Mark where platelets are.
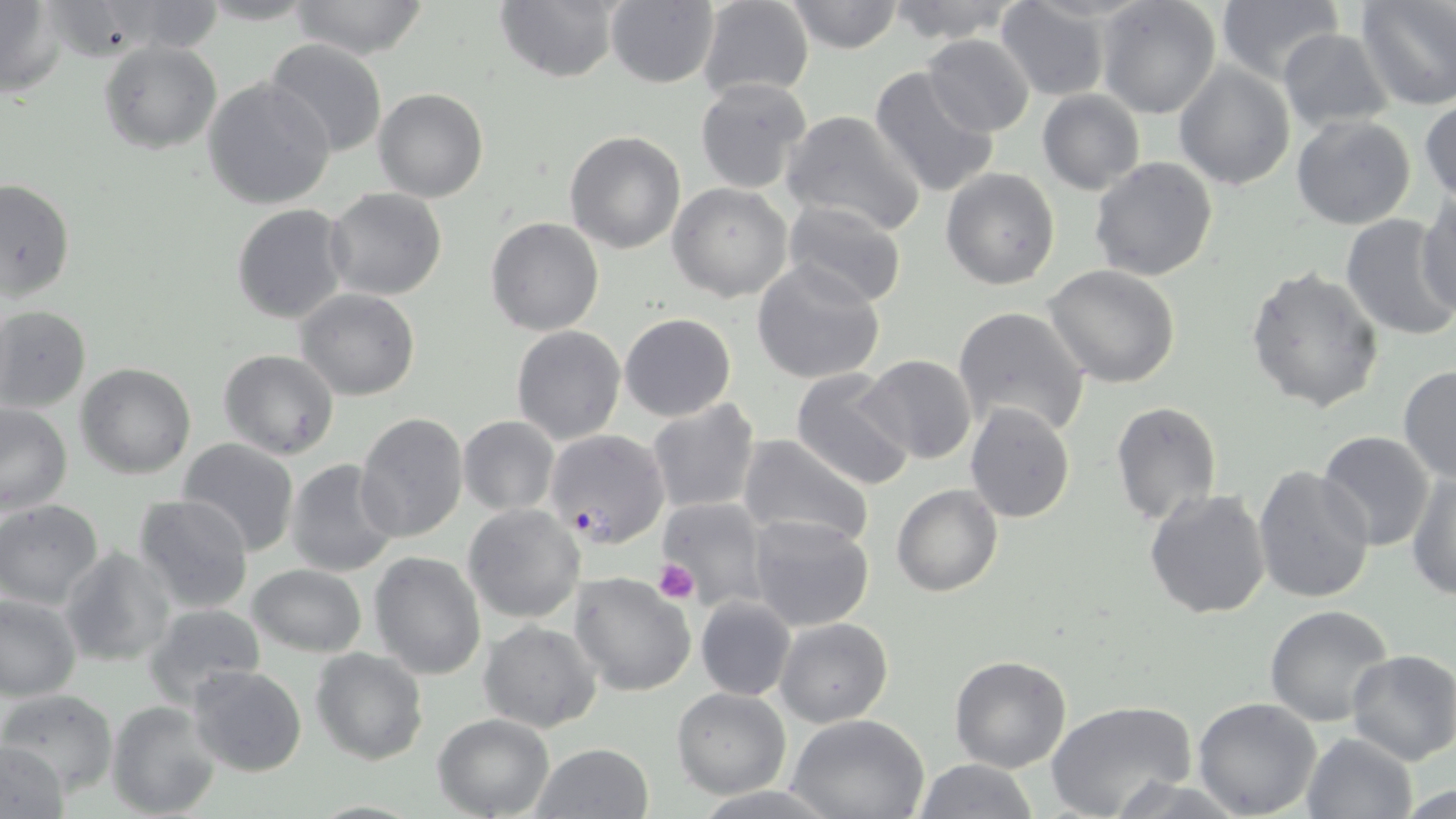

Approximate bounding boxes as [x1, y1, x2, y2] in pixels.
Platelets: [654, 559, 700, 605].

{
  "slide_level_diagnosis": "Plasmodium falciparum",
  "uninfected_red_blood_cell_locations": "approximate bounding boxes as [x1, y1, x2, y2] in pixels: [287, 0, 431, 60], [696, 0, 814, 100], [784, 0, 906, 54], [883, 0, 1023, 43], [1095, 0, 1222, 119], [1358, 0, 1455, 110], [0, 1, 63, 95], [495, 1, 620, 82], [605, 1, 720, 87], [994, 1, 1112, 102], [1216, 2, 1341, 82], [1278, 28, 1393, 130], [922, 34, 1035, 138], [98, 39, 221, 153], [262, 39, 388, 159], [1174, 62, 1294, 190], [869, 67, 1000, 199], [203, 77, 335, 211], [695, 77, 814, 193], [373, 88, 488, 202], [1037, 89, 1145, 195], [1420, 99, 1456, 201], [782, 110, 926, 236], [1291, 115, 1417, 230], [565, 131, 687, 254], [1089, 156, 1218, 282], [942, 167, 1060, 290], [0, 178, 74, 302], [667, 182, 795, 302], [325, 186, 447, 301], [1414, 193, 1455, 320], [782, 200, 909, 308], [232, 205, 348, 324], [1340, 214, 1456, 342], [485, 218, 603, 336], [752, 260, 886, 386], [1044, 265, 1183, 388], [1244, 268, 1385, 413], [296, 288, 421, 401], [952, 305, 1090, 438], [0, 306, 90, 412], [619, 313, 736, 422], [511, 326, 627, 444], [219, 349, 340, 460], [858, 356, 979, 464], [76, 363, 197, 479], [1398, 364, 1456, 483], [792, 368, 917, 491], [646, 398, 761, 516], [1110, 400, 1223, 527], [0, 402, 73, 516], [964, 402, 1076, 523], [355, 412, 468, 543], [459, 415, 559, 515], [1317, 431, 1435, 550], [736, 436, 877, 553], [178, 438, 300, 557], [284, 459, 399, 576], [1251, 466, 1376, 605], [1410, 467, 1455, 600], [892, 484, 1002, 596], [1144, 488, 1273, 620], [132, 494, 254, 616], [659, 497, 768, 607], [0, 500, 105, 609], [462, 505, 585, 622], [747, 514, 874, 631], [60, 545, 177, 667], [369, 551, 486, 680], [248, 564, 367, 657], [570, 572, 697, 696], [0, 590, 83, 700], [695, 596, 796, 701], [142, 603, 268, 709], [1264, 604, 1395, 726], [775, 616, 892, 728], [478, 621, 602, 734], [310, 648, 428, 765], [1346, 650, 1456, 766], [949, 654, 1072, 772], [186, 665, 308, 778], [672, 687, 791, 799], [2, 689, 118, 796], [1192, 696, 1323, 818], [1046, 699, 1198, 819], [107, 700, 222, 818], [433, 713, 555, 818], [788, 714, 930, 819], [1301, 732, 1418, 819], [1, 742, 70, 818], [530, 742, 654, 819], [913, 758, 1040, 819], [1398, 783, 1455, 817]",
  "modality": "light microscopy",
  "preparation": "thin blood smear",
  "magnification": "1000x",
  "stain": "May-Grünwald-Giemsa",
  "field_of_view": "one of a larger specimen",
  "image_size": "1456×819 pixels",
  "plasmodium_falciparum_infected_red_blood_cell_locations": "approximate bounding boxes as [x1, y1, x2, y2] in pixels: [544, 428, 670, 548]"
}